Assess this cell for malaria.
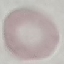

Uninfected.

{
  "capture": "smartphone camera at the microscope eyepiece",
  "preparation": "thin blood smear",
  "stain": "Giemsa",
  "image_type": "cell patch, automatically extracted from a larger field of view and resized to 64 × 64 pixels"
}